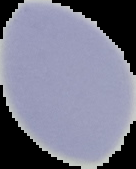

Summary:
  - Malaria status: uninfected
  - Image type: segmented cell region on a black background
  - Image size: 136×169 pixels
  - Preparation: thin blood smear